Report the malaria status of this cell.
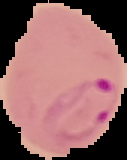

Parasitized.

From a thin blood film. Image is 127×160 pixels. The area outside the segmented cell region is set to black.